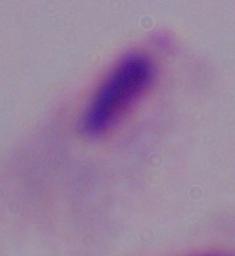

magnification = 1000x
identification = trichomonad
modality = photomicrograph